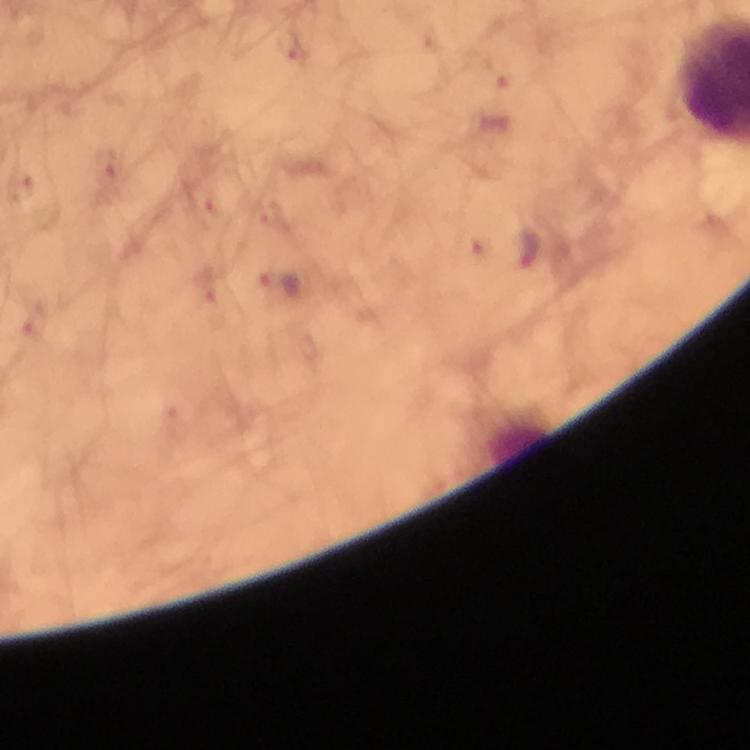

Approximate centers as [x, y] in pixels. Malaria parasite locations: [290, 44], [103, 166], [19, 192], [201, 206], [479, 247], [529, 249], [279, 285], [211, 287], [29, 318], [171, 418]. Image is 750×750 pixels. Immersion oil applied. 100x magnification. From a diagnostic examination for malaria. Cropped region of a single field of view. Thick blood smear. Giemsa-stained preparation. Smartphone photograph taken through a microscope.